Report the malaria status of this cell.
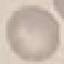

It is uninfected.

Summary:
  - Stain: Giemsa
  - Preparation: thin smear
  - Capture: smartphone through the microscope eyepiece
  - Image type: cell patch, automatically extracted from a larger field of view and resized to 64 × 64 pixels